Name the blood parasite species.
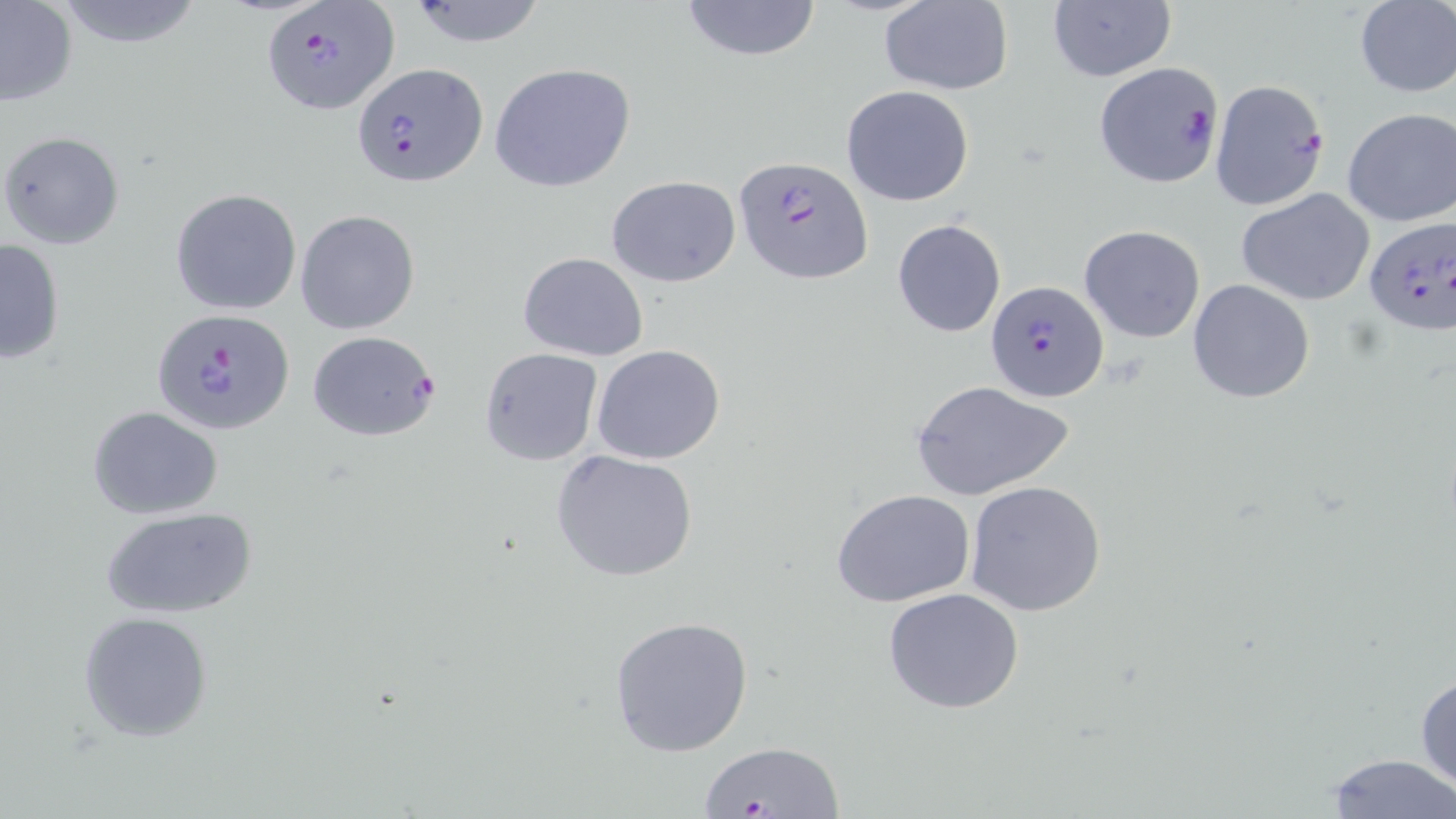
Plasmodium falciparum.

Approximate bounding boxes as (x1,y1)-(x2,y2) corner pairs in pixels. Plasmodium falciparum-infected red blood cell locations: (261,1)-(399,115), (1092,62)-(1225,189), (353,63)-(487,187), (1209,80)-(1330,211), (733,155)-(872,286), (1363,217)-(1456,341), (985,280)-(1107,402), (152,308)-(295,437), (305,329)-(441,443). Uninfected red blood cell locations: (48,0)-(207,49), (404,0)-(552,48), (676,0)-(823,63), (878,1)-(1013,96), (1352,1)-(1456,97), (0,2)-(78,107), (1047,2)-(1177,83), (488,62)-(636,194), (841,85)-(976,207), (1340,107)-(1454,228), (0,130)-(126,250), (605,174)-(741,287), (170,188)-(303,316), (1237,188)-(1376,307), (295,210)-(420,334), (891,218)-(1006,338), (1079,225)-(1205,343), (0,237)-(67,364), (519,252)-(648,361), (1187,279)-(1314,403), (591,345)-(726,465), (478,346)-(603,465), (911,380)-(1073,503), (86,407)-(224,518), (552,449)-(699,583), (966,480)-(1108,617), (831,490)-(975,608), (101,507)-(260,621), (882,588)-(1026,715), (78,611)-(215,742), (608,616)-(754,758), (1415,665)-(1456,799), (693,740)-(849,819), (1326,753)-(1452,817). Image is 1456×819 pixels. Thin blood smear. May-Grünwald-Giemsa-stained preparation. Single field of view. 1000x magnification. Optical microscopy.